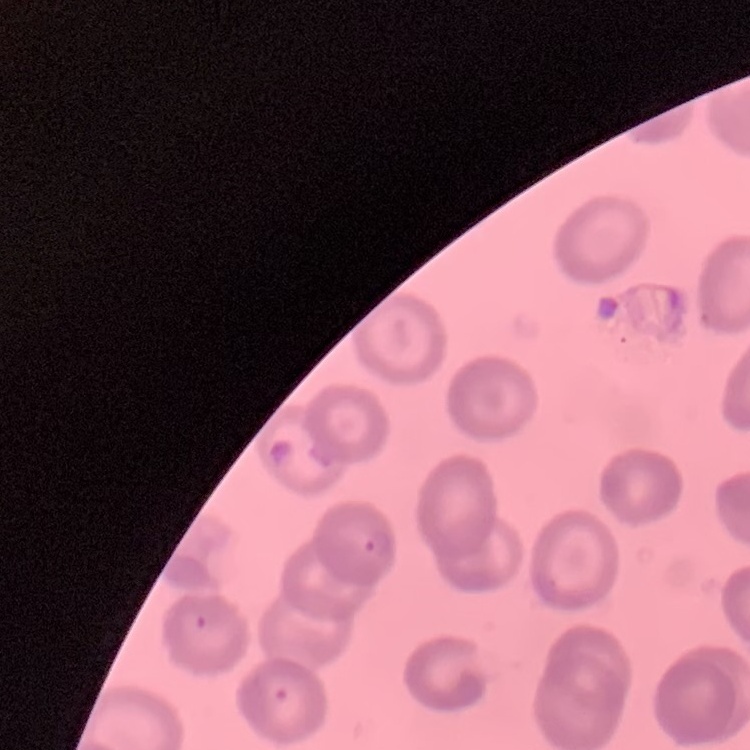
Summary:
  - Red blood cell morphology: no rouleaux formation
  - Preparation: thin blood smear
  - Image type: one tile cut from a larger photomicrograph
  - Stain: Field's or Giemsa